Assess this cell for malaria.
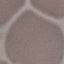

Uninfected.

Summary:
  - Image type: automatically extracted cell patch, resized to 64 × 64 pixels
  - Capture: smartphone camera at the microscope eyepiece
  - Preparation: thin smear
  - Stain: Giemsa